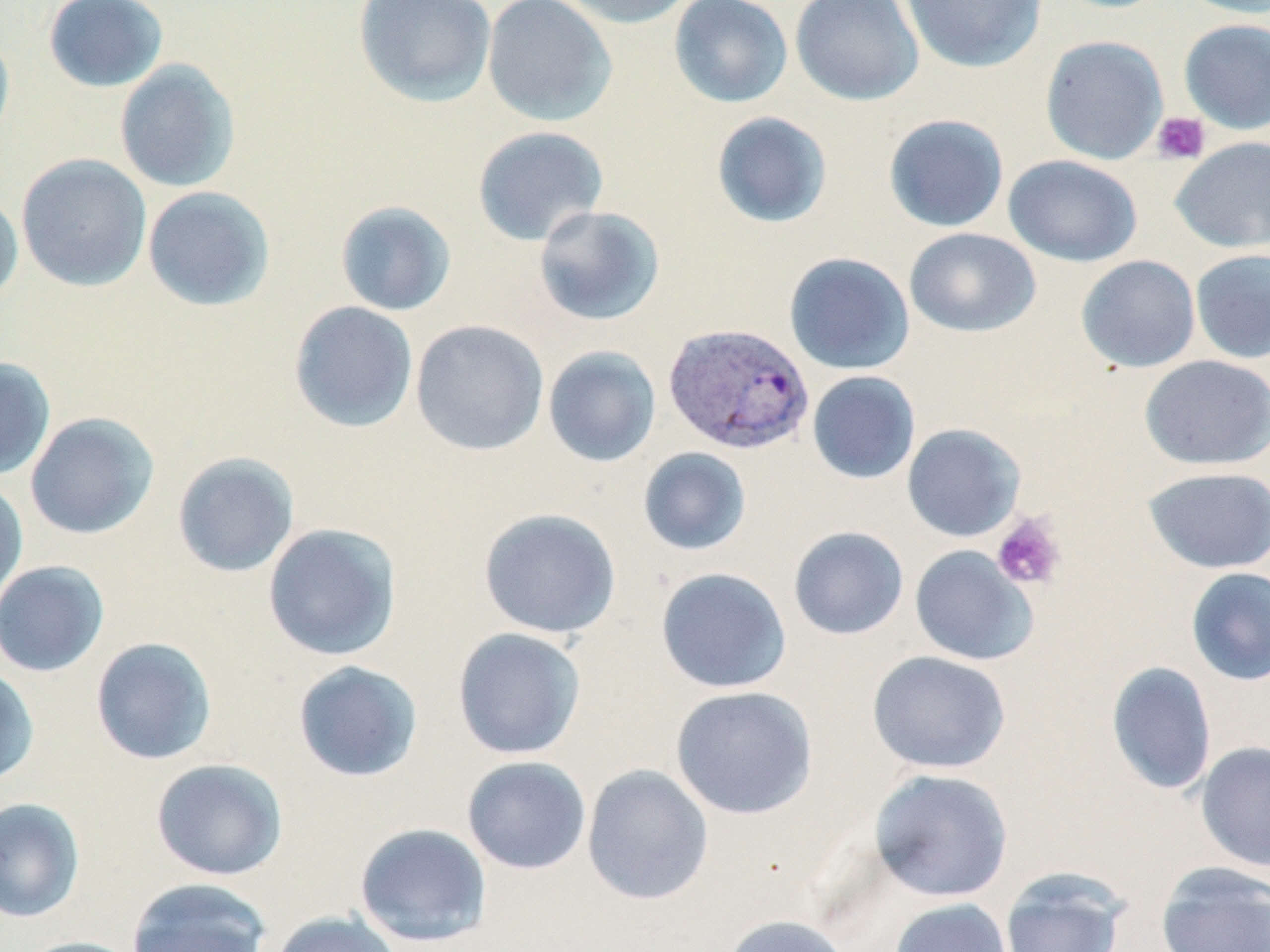

Summary:
  - Coordinate format: approximate bounding boxes as named x1/y1/x2/y2 corners in pixels
  - Plasmodium vivax-infected red blood cell locations: (x1=663, y1=322, x2=816, y2=455)
  - Platelet locations: (x1=1152, y1=111, x2=1210, y2=165), (x1=991, y1=513, x2=1066, y2=592)
  - Uninfected red blood cell locations: (x1=43, y1=0, x2=169, y2=93), (x1=353, y1=0, x2=497, y2=108), (x1=481, y1=0, x2=618, y2=127), (x1=557, y1=0, x2=698, y2=29), (x1=669, y1=0, x2=793, y2=108), (x1=790, y1=0, x2=924, y2=106), (x1=899, y1=0, x2=1047, y2=74), (x1=1179, y1=0, x2=1270, y2=19), (x1=1179, y1=18, x2=1270, y2=134), (x1=0, y1=28, x2=15, y2=154), (x1=1040, y1=35, x2=1168, y2=164), (x1=114, y1=60, x2=241, y2=193), (x1=711, y1=112, x2=833, y2=229), (x1=883, y1=114, x2=1009, y2=233), (x1=472, y1=126, x2=609, y2=247), (x1=1170, y1=136, x2=1270, y2=253), (x1=16, y1=153, x2=152, y2=292), (x1=1003, y1=154, x2=1143, y2=267), (x1=142, y1=185, x2=275, y2=312), (x1=0, y1=191, x2=24, y2=307), (x1=335, y1=201, x2=457, y2=316), (x1=534, y1=205, x2=666, y2=326), (x1=903, y1=227, x2=1041, y2=337), (x1=1190, y1=249, x2=1270, y2=363), (x1=783, y1=251, x2=915, y2=375), (x1=1076, y1=255, x2=1201, y2=373), (x1=288, y1=301, x2=419, y2=433), (x1=410, y1=319, x2=549, y2=456), (x1=542, y1=345, x2=661, y2=468), (x1=1139, y1=355, x2=1269, y2=470), (x1=0, y1=357, x2=56, y2=480), (x1=807, y1=371, x2=921, y2=484), (x1=25, y1=411, x2=160, y2=540), (x1=902, y1=423, x2=1026, y2=542), (x1=637, y1=447, x2=752, y2=556), (x1=172, y1=452, x2=300, y2=578), (x1=1141, y1=466, x2=1270, y2=574), (x1=0, y1=477, x2=29, y2=609), (x1=478, y1=507, x2=622, y2=639), (x1=262, y1=522, x2=402, y2=662), (x1=788, y1=526, x2=909, y2=640), (x1=909, y1=545, x2=1039, y2=666), (x1=0, y1=560, x2=110, y2=677), (x1=655, y1=567, x2=792, y2=694), (x1=1185, y1=567, x2=1270, y2=686), (x1=452, y1=627, x2=587, y2=760), (x1=90, y1=636, x2=218, y2=765), (x1=866, y1=650, x2=1012, y2=774), (x1=292, y1=660, x2=423, y2=783), (x1=1106, y1=661, x2=1217, y2=795), (x1=0, y1=665, x2=39, y2=788), (x1=670, y1=685, x2=818, y2=820), (x1=1195, y1=741, x2=1270, y2=872), (x1=462, y1=756, x2=592, y2=875), (x1=150, y1=758, x2=288, y2=881), (x1=581, y1=764, x2=714, y2=905), (x1=869, y1=768, x2=1014, y2=902), (x1=0, y1=797, x2=85, y2=923), (x1=353, y1=822, x2=493, y2=948), (x1=1154, y1=862, x2=1270, y2=952), (x1=999, y1=869, x2=1130, y2=952), (x1=126, y1=878, x2=272, y2=952), (x1=889, y1=898, x2=1014, y2=952), (x1=268, y1=910, x2=403, y2=952), (x1=719, y1=914, x2=852, y2=952), (x1=15, y1=936, x2=146, y2=952)
  - Slide-level diagnosis: Plasmodium vivax
  - Modality: optical microscopy
  - Stain: May-Grünwald-Giemsa
  - Preparation: thin blood smear
  - Field of view: single
  - Image size: 1270×952 pixels
  - Magnification: 1000x